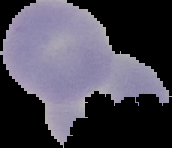
Summary:
  - Image size: 172×148 pixels
  - Malaria status: uninfected
  - Preparation: thin blood smear
  - Image type: segmented cell region on a black background